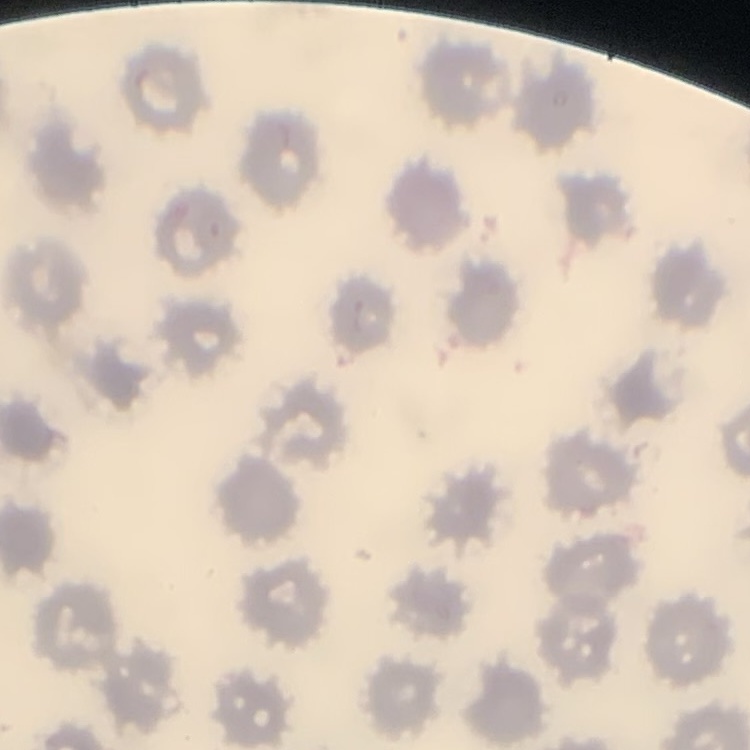

erythrocyte morphology = no rouleaux formation
image type = one tile cut from a larger photomicrograph
preparation = thin blood smear
stain = Field's or Giemsa